Assess this cell for malaria.
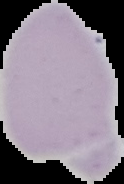

Uninfected.

{
  "image_size": "124×184 pixels",
  "preparation": "thin blood film",
  "image_type": "cell region segmented out of the field of view; surrounding area masked to black"
}